Classify this cell by malaria status.
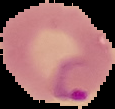
Parasitized.

The area outside the segmented cell region is set to black. From a thin blood film. Image is 115×109 pixels.